Point out each Plasmodium parasite.
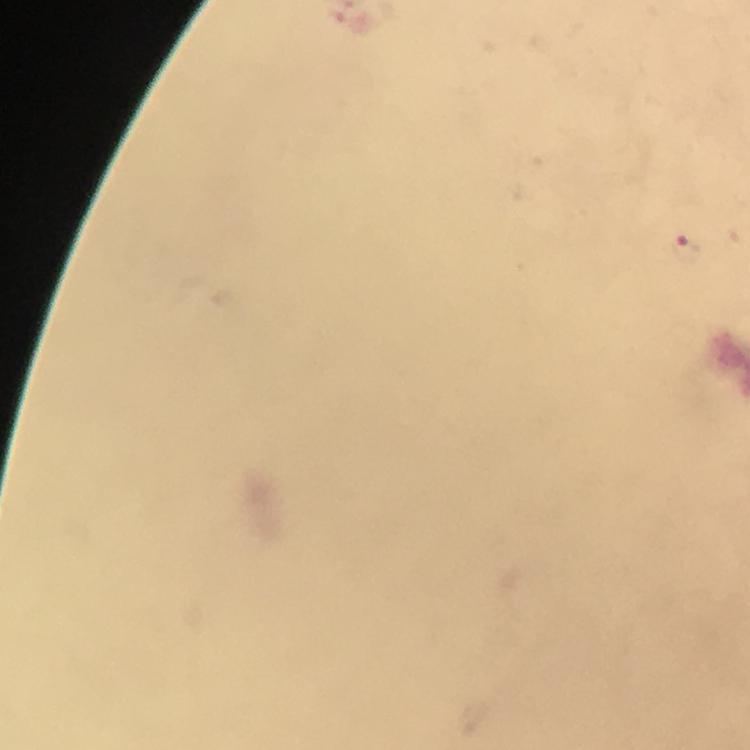

Approximate centers as [x, y] in pixels.
Plasmodium parasites: [686, 246].

stain = Giemsa
context = from a malaria diagnostic workup
cropped from = a single field of view
magnification = 100x
immersion oil = applied
image size = 750×750 pixels
capture = smartphone photograph through a microscope
preparation = thick smear